Assess for malaria.
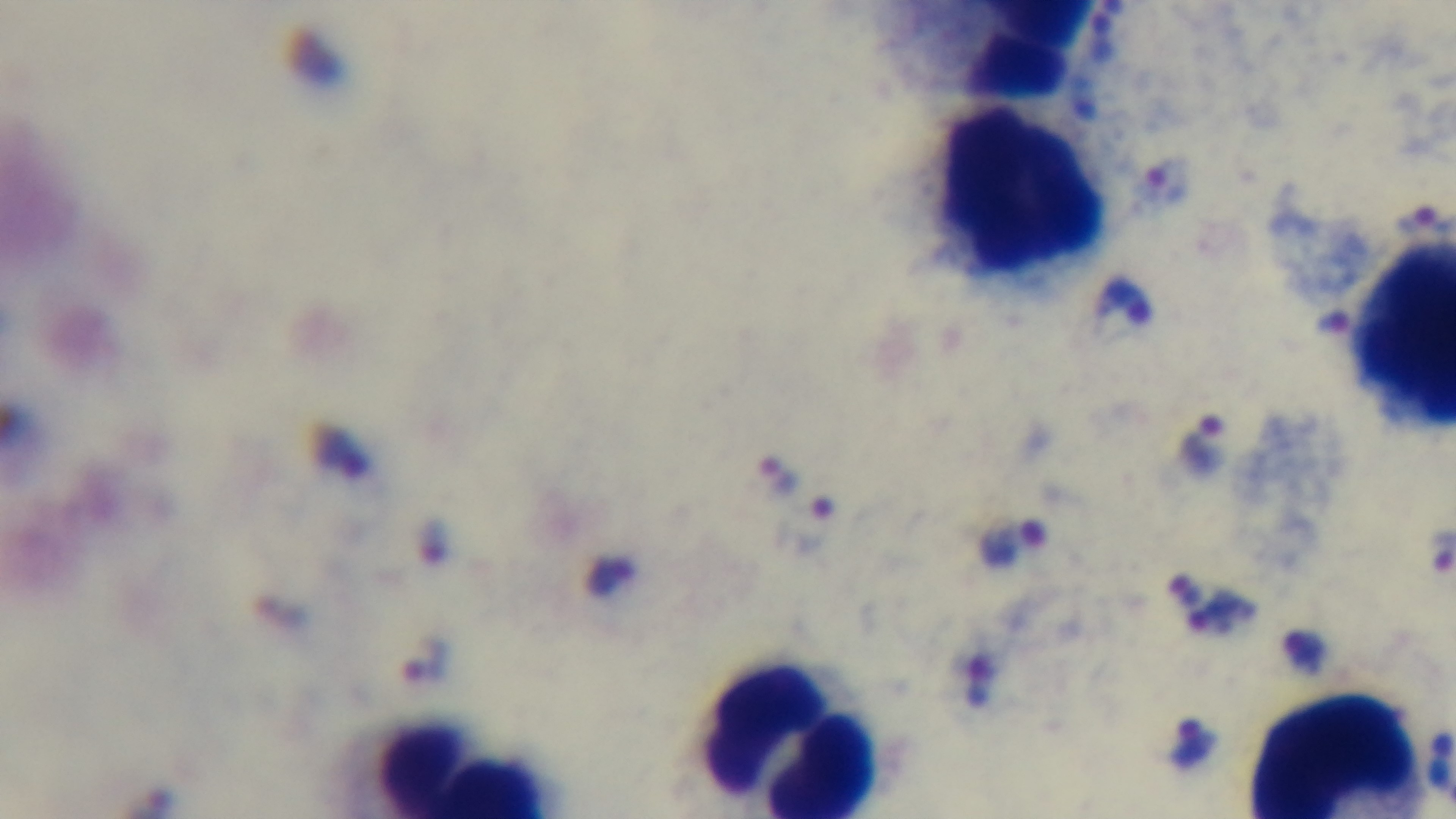
Infected.

{
  "stain": "Giemsa",
  "capture": "mounted 4K digital camera",
  "preparation": "thick blood film",
  "modality": "light microscopy",
  "objective": "100x oil immersion",
  "field_of_view": "single"
}